Report the malaria status of this cell.
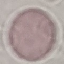

It is uninfected.

{
  "stain": "Giemsa",
  "preparation": "thin smear",
  "image_type": "automatically extracted cell patch, resized to 64 × 64 pixels",
  "capture": "smartphone through the microscope eyepiece"
}